Report the malaria status of this cell.
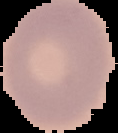

It is uninfected.

Summary:
  - Image type: segmented cell region with the area outside set to black
  - Preparation: thin blood smear
  - Image size: 118×133 pixels